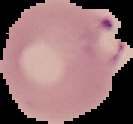
preparation = thin blood smear
image size = 133×124 pixels
result = malaria parasites detected
image type = segmented cell region on a black background